Assess this cell for malaria.
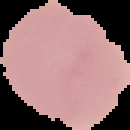
It is uninfected.

From a thin blood smear. Image is 130×130 pixels. Cell region segmented out of the field of view; the surrounding area is masked to black.